Describe the morphology of the erythrocytes.
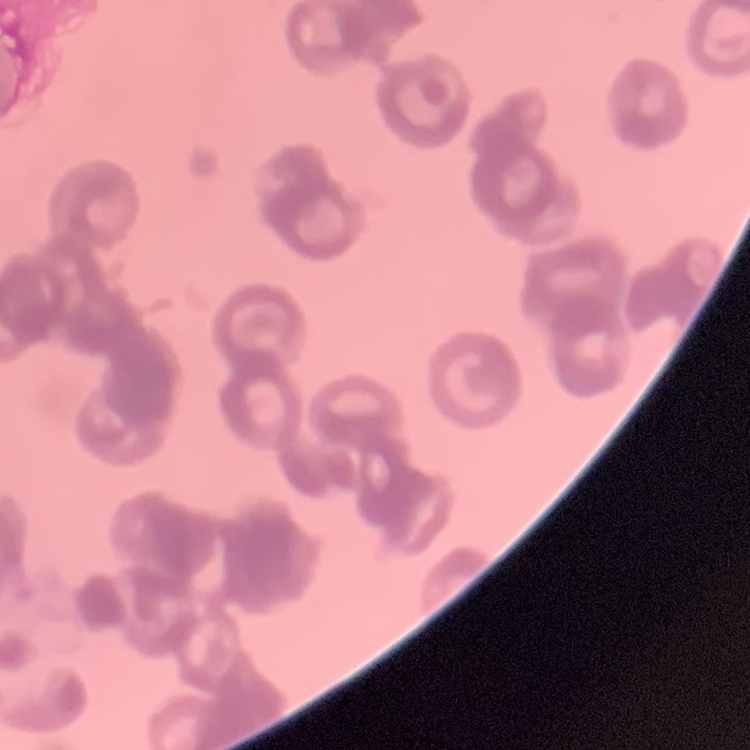

They show rouleaux formation.

One tile cut from a larger photomicrograph. Field's or Giemsa stain. Thin peripheral smear.